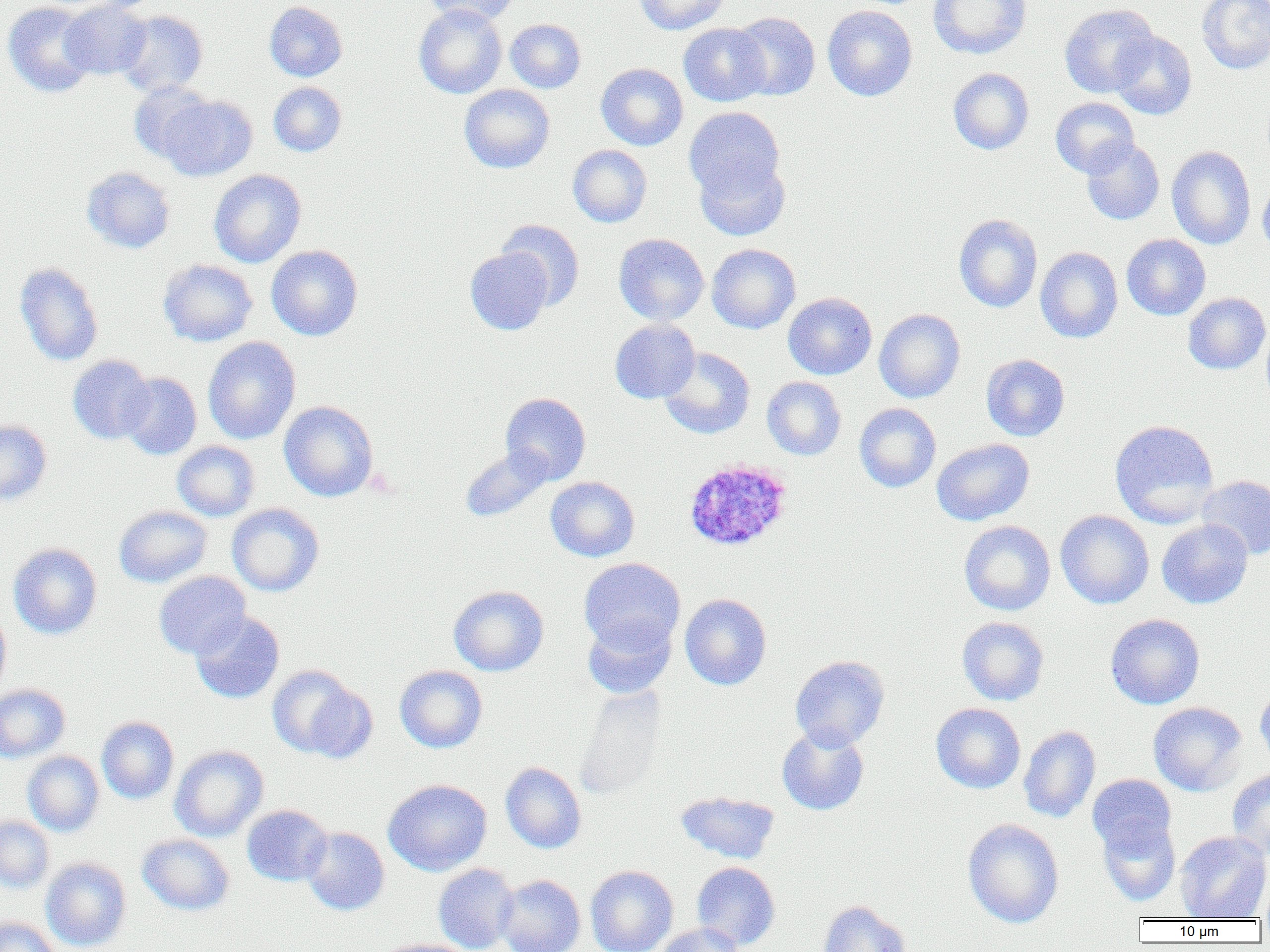

slide_level_diagnosis: Plasmodium ovale
field_of_view: one of a larger specimen
plasmodium_ovale_infected_red_blood_cell_locations: 'approximate bounding boxes as (x1, y1, x2, y2) in pixels: (683, 459, 792, 552)'
image_size: 1270×952 pixels
uninfected_red_blood_cell_locations: 'approximate bounding boxes as (x1, y1, x2, y2) in pixels: (60, 0, 152, 80), (423, 0, 519, 26), (634, 0, 729, 35), (929, 0, 1032, 59), (1196, 0, 1270, 74), (2, 1, 98, 97), (264, 2, 347, 81), (413, 4, 507, 99), (1059, 4, 1158, 99), (822, 5, 917, 101), (116, 10, 208, 96), (730, 11, 821, 100), (505, 19, 586, 92), (678, 23, 771, 106), (1109, 30, 1196, 120), (596, 63, 688, 150), (948, 68, 1034, 155), (129, 81, 214, 162), (268, 82, 347, 156), (459, 84, 555, 173), (160, 94, 257, 181), (1050, 97, 1139, 178), (683, 106, 786, 206), (1081, 137, 1165, 225), (567, 144, 652, 227), (1167, 146, 1256, 250), (694, 152, 791, 241), (81, 167, 175, 253), (209, 169, 306, 268), (1258, 176, 1270, 258), (954, 214, 1042, 312), (497, 219, 585, 309), (613, 233, 709, 325), (1122, 234, 1211, 320), (707, 244, 801, 334), (266, 245, 363, 340), (465, 247, 554, 335), (1036, 247, 1123, 343), (158, 259, 258, 346), (14, 262, 104, 366), (782, 292, 877, 380), (1183, 293, 1270, 374), (874, 309, 966, 403), (610, 319, 700, 403), (1261, 320, 1270, 410), (203, 337, 300, 444), (659, 347, 755, 439), (981, 354, 1070, 441), (67, 355, 155, 444), (118, 372, 202, 460), (762, 376, 847, 460), (500, 392, 591, 484), (279, 400, 378, 502), (854, 403, 941, 492), (1109, 419, 1220, 528), (0, 420, 52, 506), (931, 438, 1034, 526), (172, 441, 260, 521), (461, 446, 554, 522), (1196, 475, 1270, 560), (545, 476, 640, 562), (226, 503, 325, 596), (114, 505, 211, 588), (1055, 510, 1154, 609), (1157, 519, 1253, 609), (959, 520, 1055, 615), (8, 543, 102, 639), (578, 558, 685, 655), (153, 571, 251, 659), (448, 585, 549, 676), (680, 593, 771, 690), (0, 606, 11, 700), (190, 610, 284, 703), (582, 613, 677, 698), (1106, 613, 1205, 709), (957, 617, 1049, 706), (789, 655, 889, 750), (266, 665, 370, 761), (395, 665, 487, 753), (1255, 682, 1270, 773), (0, 684, 70, 763), (574, 686, 669, 800), (931, 702, 1026, 793), (1148, 702, 1247, 796), (97, 716, 179, 804), (776, 725, 869, 816), (1019, 726, 1101, 823), (170, 745, 268, 841), (23, 751, 104, 836), (500, 762, 587, 853), (1227, 768, 1270, 858), (1088, 773, 1176, 856), (383, 779, 492, 876), (675, 791, 780, 864), (242, 805, 332, 886), (0, 816, 54, 893), (1097, 817, 1180, 906), (962, 818, 1064, 928), (301, 827, 389, 915), (1174, 831, 1270, 920), (137, 834, 234, 915), (41, 857, 131, 951), (691, 862, 780, 951), (433, 864, 519, 952), (585, 865, 678, 952), (496, 875, 585, 952), (818, 900, 912, 952), (0, 916, 60, 952), (654, 923, 745, 952), (374, 939, 476, 952)'
preparation: thin blood film
modality: optical microscopy
magnification: 1000x